Give the position of every Plasmodium parasite.
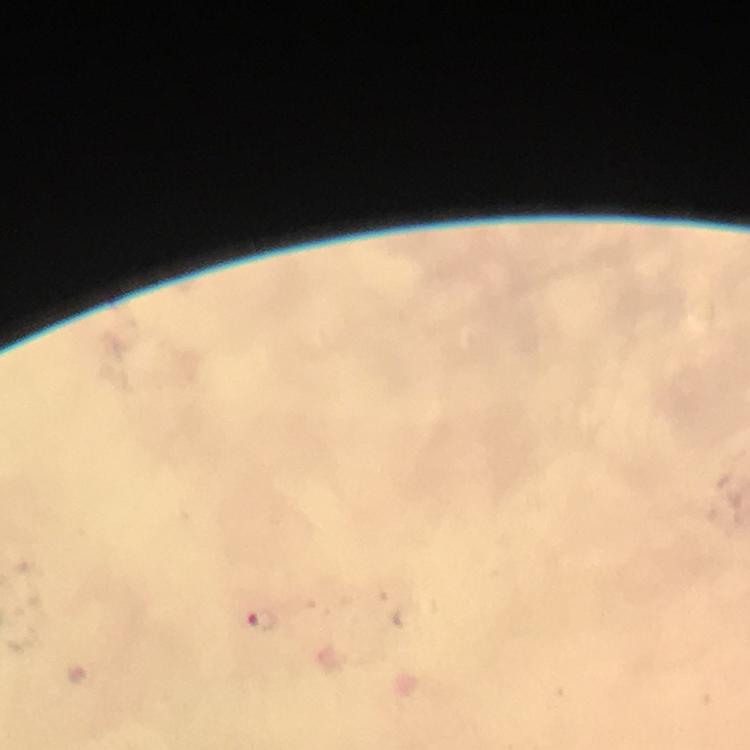

Approximate object centers, in pixels from the top-left corner.
Plasmodium parasites: (x=261, y=624).

{
  "immersion_oil": "applied",
  "preparation": "thick smear",
  "context": "from a diagnostic examination for malaria",
  "capture": "smartphone mounted on the microscope",
  "cropped_from": "one field of view",
  "magnification": "100x",
  "stain": "Giemsa",
  "image_size": "750×750 pixels"
}